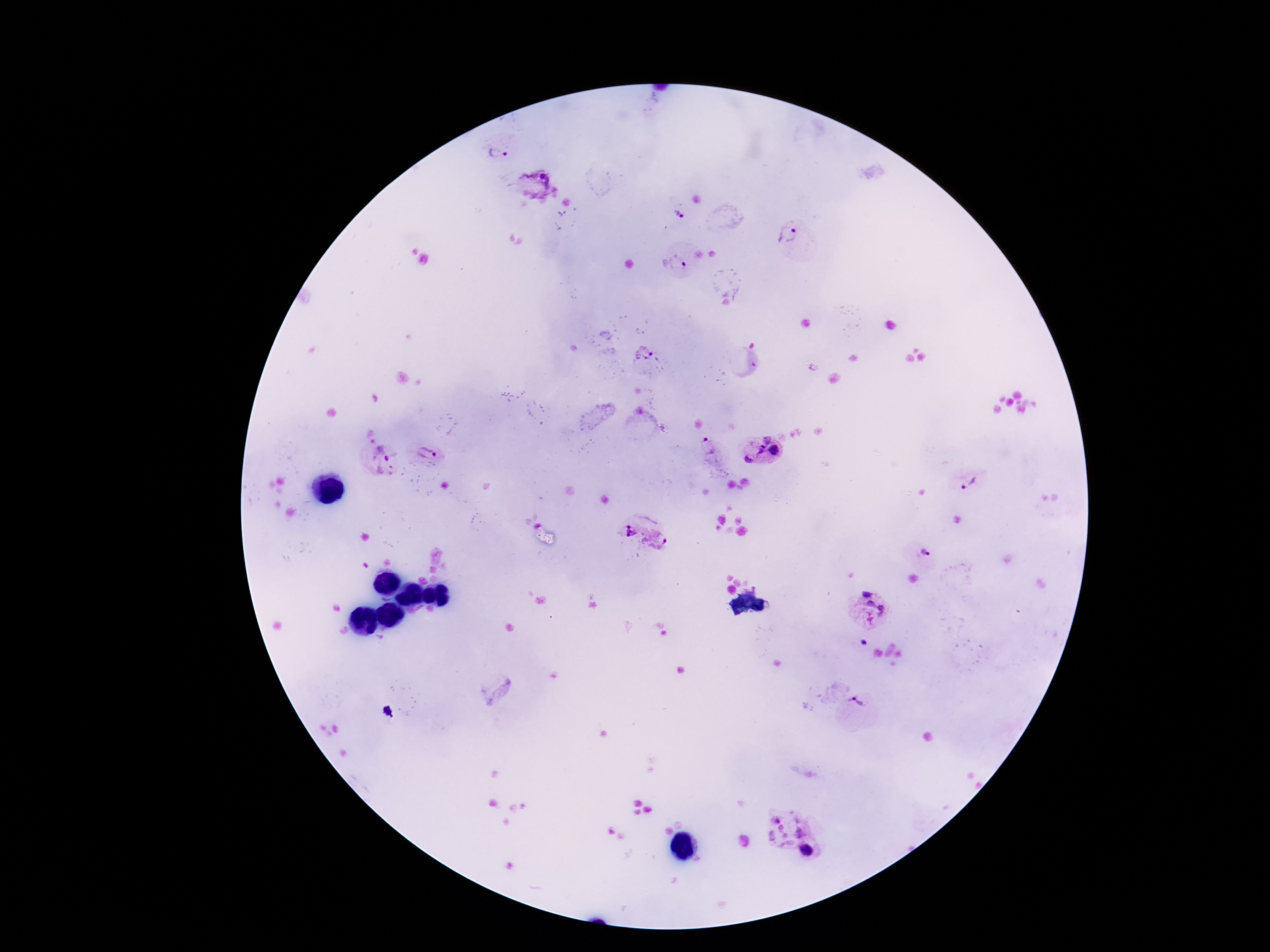 Approximate centers as (x, y) in pixels. Plasmodium parasite locations: (497, 153), (537, 187), (678, 216), (787, 235), (674, 265), (644, 356), (747, 357), (760, 443), (709, 450), (775, 451), (428, 452), (381, 460), (748, 460), (968, 481), (628, 530), (657, 539), (925, 553), (867, 609), (862, 642), (856, 702), (388, 712), (784, 825), (808, 852). Image is 1270×952 pixels. Photographed through the microscope eyepiece with a smartphone camera. Thick blood film. Patient malaria status: positive. One field from this slide. Giemsa-stained preparation. 100x magnification.